State the blood parasite species.
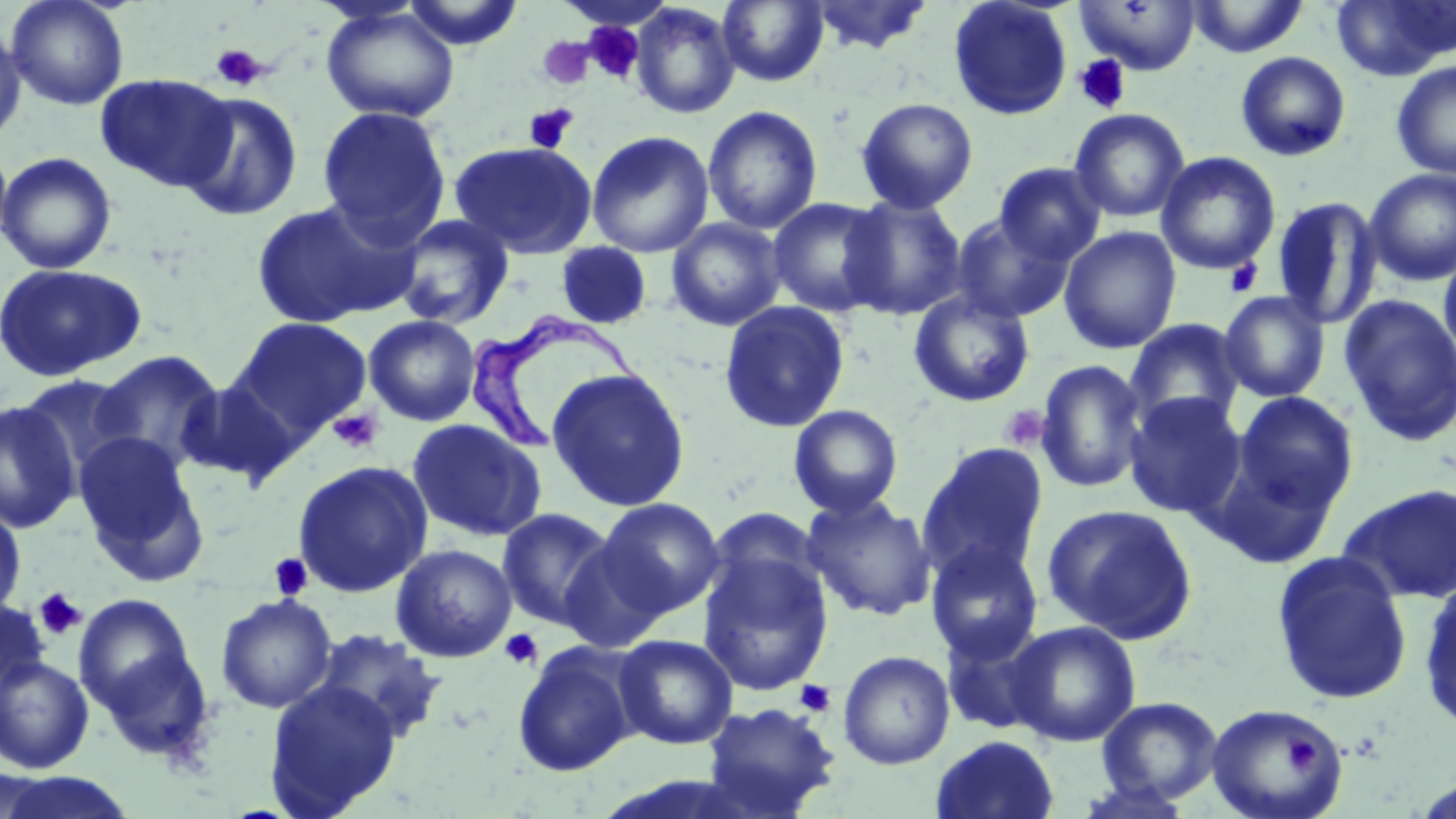

Trypanosoma brucei.

Summary:
  - Coordinate format: approximate bounding boxes as named x1/y1/x2/y2 corners in pixels
  - Uninfected red blood cell locations: (x1=5, y1=0, x2=130, y2=111), (x1=401, y1=0, x2=525, y2=50), (x1=718, y1=0, x2=829, y2=86), (x1=805, y1=0, x2=935, y2=55), (x1=948, y1=0, x2=1073, y2=121), (x1=1073, y1=0, x2=1201, y2=75), (x1=1186, y1=0, x2=1310, y2=58), (x1=1331, y1=0, x2=1456, y2=80), (x1=630, y1=3, x2=741, y2=119), (x1=321, y1=5, x2=461, y2=123), (x1=0, y1=21, x2=26, y2=144), (x1=1235, y1=51, x2=1351, y2=162), (x1=1391, y1=61, x2=1456, y2=179), (x1=96, y1=74, x2=236, y2=191), (x1=178, y1=92, x2=303, y2=222), (x1=855, y1=97, x2=979, y2=213), (x1=702, y1=105, x2=823, y2=235), (x1=316, y1=106, x2=452, y2=246), (x1=1069, y1=108, x2=1191, y2=223), (x1=586, y1=130, x2=714, y2=258), (x1=0, y1=137, x2=14, y2=255), (x1=449, y1=141, x2=598, y2=258), (x1=0, y1=151, x2=116, y2=274), (x1=1156, y1=151, x2=1280, y2=275), (x1=994, y1=162, x2=1106, y2=265), (x1=1365, y1=169, x2=1456, y2=286), (x1=840, y1=196, x2=967, y2=320), (x1=1270, y1=196, x2=1382, y2=329), (x1=768, y1=197, x2=890, y2=317), (x1=250, y1=199, x2=412, y2=329), (x1=950, y1=213, x2=1074, y2=324), (x1=392, y1=214, x2=515, y2=330), (x1=666, y1=217, x2=787, y2=332), (x1=1058, y1=226, x2=1182, y2=354), (x1=556, y1=242, x2=653, y2=330), (x1=1439, y1=247, x2=1456, y2=371), (x1=0, y1=263, x2=147, y2=382), (x1=908, y1=289, x2=1035, y2=407), (x1=1219, y1=291, x2=1330, y2=402), (x1=1339, y1=294, x2=1456, y2=445), (x1=718, y1=300, x2=850, y2=433), (x1=363, y1=314, x2=481, y2=426), (x1=232, y1=317, x2=373, y2=440), (x1=1124, y1=319, x2=1246, y2=431), (x1=91, y1=350, x2=226, y2=473), (x1=1035, y1=359, x2=1148, y2=494), (x1=546, y1=367, x2=691, y2=512), (x1=16, y1=373, x2=138, y2=483), (x1=177, y1=378, x2=301, y2=486), (x1=1123, y1=392, x2=1247, y2=519), (x1=1233, y1=392, x2=1359, y2=513), (x1=0, y1=399, x2=82, y2=534), (x1=788, y1=404, x2=904, y2=518), (x1=407, y1=418, x2=547, y2=542), (x1=73, y1=434, x2=205, y2=576), (x1=917, y1=441, x2=1049, y2=581), (x1=293, y1=460, x2=433, y2=598), (x1=1339, y1=482, x2=1456, y2=604), (x1=800, y1=495, x2=936, y2=622), (x1=596, y1=498, x2=725, y2=618), (x1=0, y1=503, x2=26, y2=622), (x1=1042, y1=504, x2=1198, y2=644), (x1=497, y1=508, x2=617, y2=630), (x1=559, y1=538, x2=670, y2=653), (x1=925, y1=541, x2=1045, y2=664), (x1=390, y1=543, x2=517, y2=663), (x1=697, y1=551, x2=834, y2=695), (x1=1270, y1=551, x2=1413, y2=706), (x1=1418, y1=579, x2=1456, y2=732), (x1=74, y1=593, x2=207, y2=740), (x1=215, y1=593, x2=338, y2=713), (x1=0, y1=597, x2=49, y2=705), (x1=1005, y1=621, x2=1141, y2=747), (x1=310, y1=628, x2=447, y2=746), (x1=614, y1=634, x2=738, y2=750), (x1=512, y1=643, x2=638, y2=777), (x1=838, y1=650, x2=955, y2=769), (x1=0, y1=656, x2=95, y2=773), (x1=263, y1=679, x2=403, y2=817), (x1=1096, y1=695, x2=1224, y2=806), (x1=701, y1=701, x2=841, y2=817), (x1=1206, y1=703, x2=1348, y2=819), (x1=930, y1=735, x2=1060, y2=819), (x1=0, y1=772, x2=140, y2=819), (x1=1073, y1=778, x2=1199, y2=819)
  - Trypanosoma brucei locations: (x1=466, y1=313, x2=625, y2=454)
  - Platelet locations: (x1=584, y1=22, x2=645, y2=83), (x1=537, y1=37, x2=594, y2=90), (x1=210, y1=43, x2=269, y2=91), (x1=1073, y1=54, x2=1132, y2=115), (x1=524, y1=103, x2=578, y2=154), (x1=1225, y1=258, x2=1263, y2=297), (x1=1000, y1=404, x2=1050, y2=452), (x1=327, y1=408, x2=384, y2=454), (x1=269, y1=552, x2=313, y2=601), (x1=34, y1=587, x2=87, y2=640), (x1=500, y1=628, x2=543, y2=670), (x1=795, y1=680, x2=836, y2=717), (x1=1283, y1=733, x2=1321, y2=774)
  - Magnification: 1000x
  - Image size: 1456×819 pixels
  - Modality: light microscopy
  - Field of view: one of a larger specimen
  - Preparation: thin blood smear
  - Stain: May-Grünwald-Giemsa